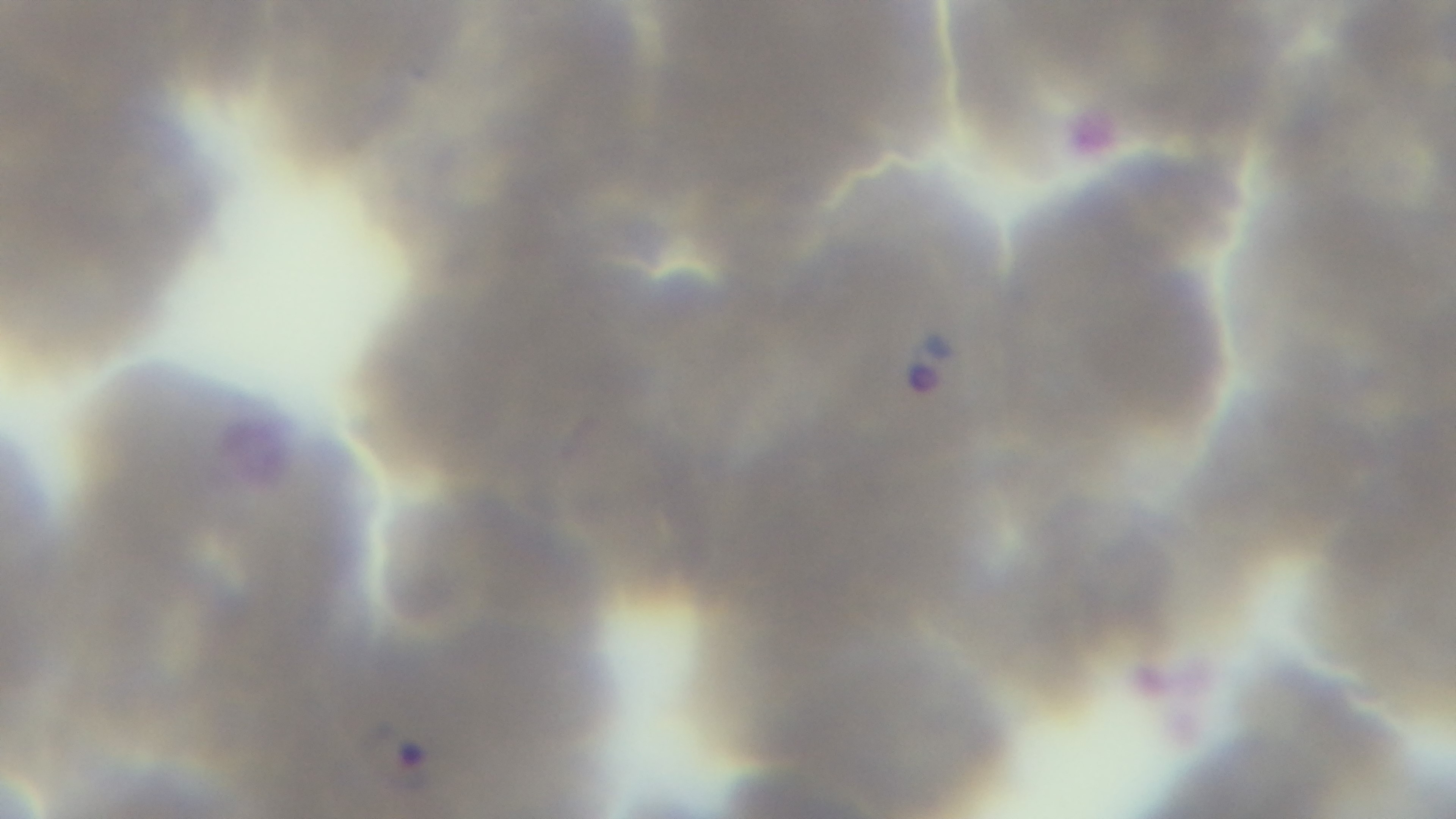
Single field of view. Malaria status: positive. Oil-immersion objective, 100x. Light microscopy. Giemsa-stained. Mounted 4K digital camera. Preparation: thin blood film.